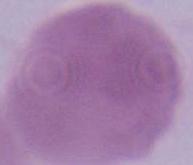

modality = micrograph
identification = red blood cell
magnification = 1000x